Comment on the morphology of the red blood cells.
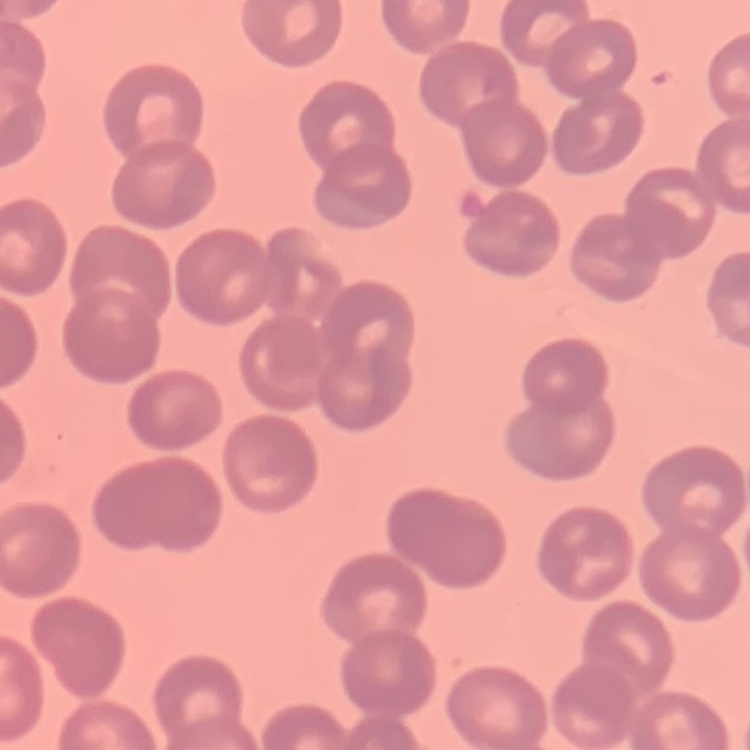

No rouleaux formation.

Summary:
  - Stain: Field's or Giemsa
  - Preparation: thin blood smear
  - Image type: one tile cut from a larger photomicrograph